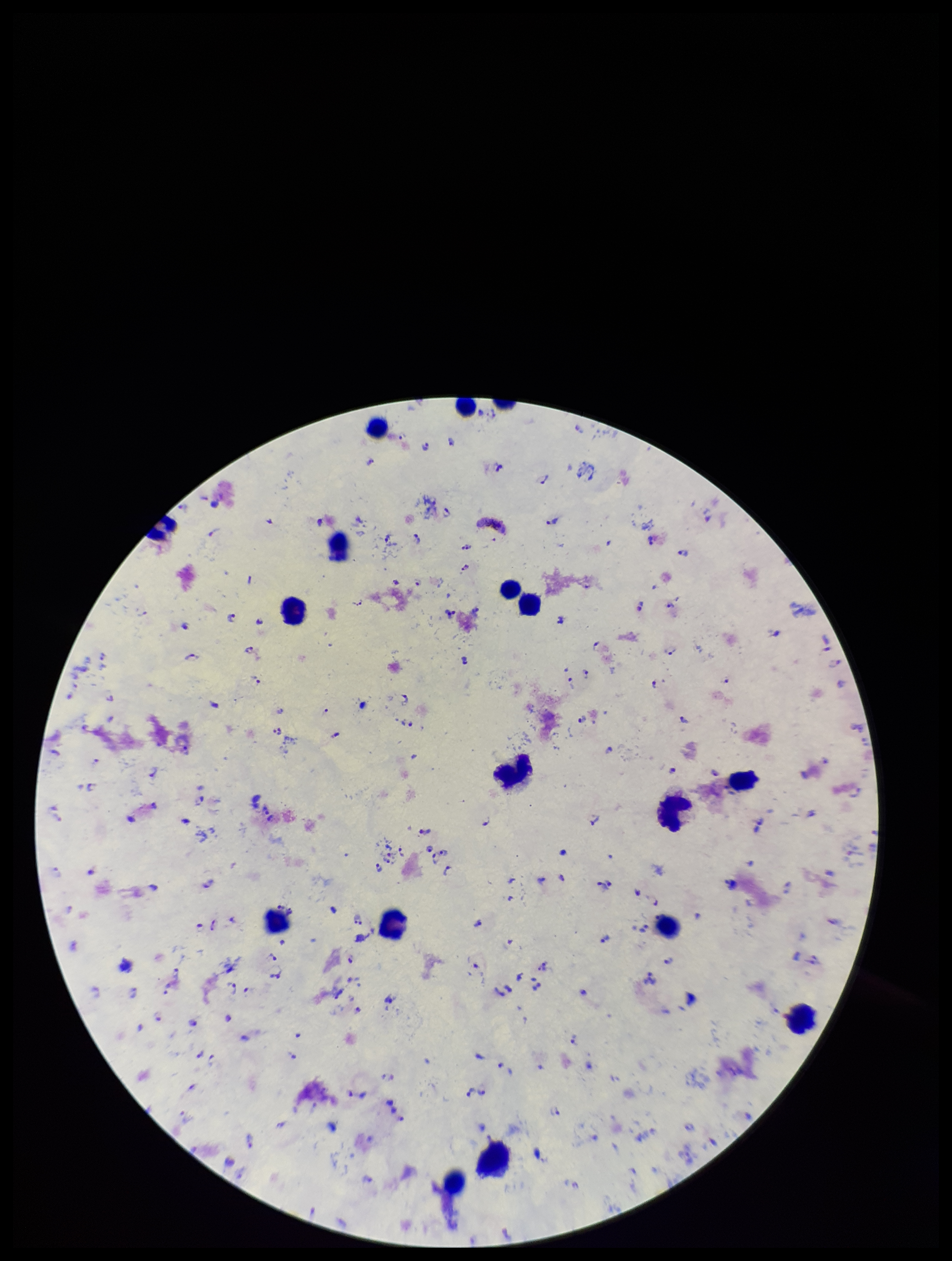
Summary:
  - Image size: 952×1261 pixels
  - Leukocyte count: 17
  - Species reported for this patient: Plasmodium falciparum
  - Preparation: thick
  - Stain: Giemsa
  - Field of view: single
  - Parasite count: 123
  - Patient malaria status: infected
  - Capture: smartphone photograph through the microscope eyepiece
  - Plasmodium parasites: identified